Give the position of every leukocyte visible.
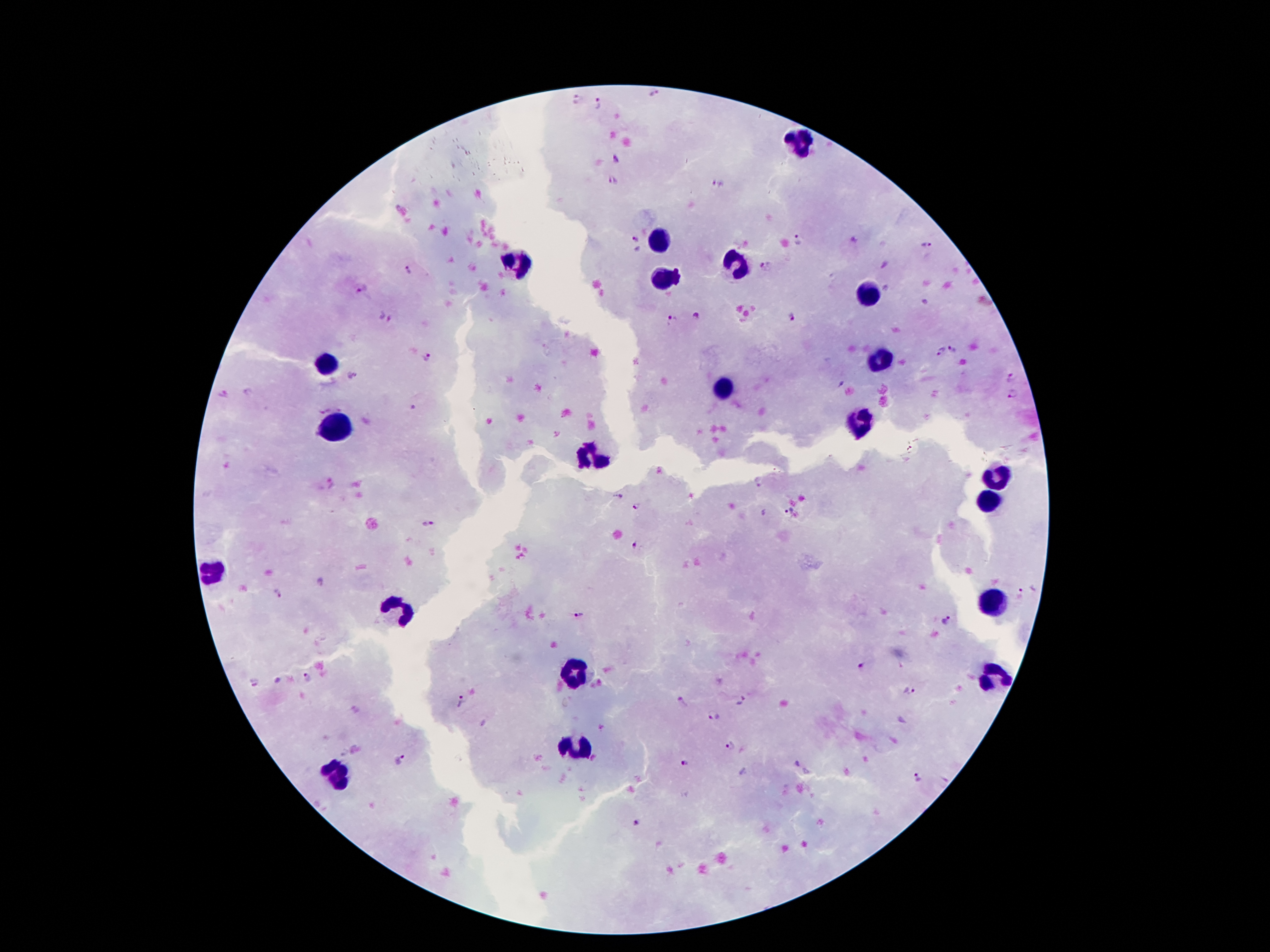
Approximate centers as [x, y] in pixels.
Leukocytes: [801, 142], [660, 241], [515, 260], [738, 262], [664, 279], [864, 293], [881, 359], [326, 365], [723, 386], [862, 422], [337, 430], [589, 459], [998, 476], [986, 502], [213, 569], [992, 604], [396, 611], [572, 670], [992, 678], [580, 743], [331, 773].

Plasmodium parasite locations = [654, 94], [577, 98], [599, 105], [616, 161], [612, 181], [717, 183], [633, 239], [800, 241], [927, 243], [765, 267], [409, 270], [363, 290], [695, 317], [385, 318], [795, 319], [672, 320], [952, 348], [941, 351], [427, 356], [351, 375], [1010, 376], [1011, 395], [412, 406], [758, 483], [620, 497], [637, 505], [789, 510], [430, 524], [636, 546], [321, 583], [278, 594], [1021, 594], [576, 615], [948, 620], [863, 667], [309, 676], [255, 679], [911, 689], [742, 700], [463, 702], [684, 702], [714, 717], [729, 745], [401, 760], [685, 762], [917, 778], [637, 824]
stain = Giemsa
image size = 1270×952 pixels
capture = smartphone camera through the microscope eyepiece
preparation = thick peripheral-blood smear
field of view = single
patient malaria status = infected with Plasmodium falciparum
magnification = 100x